Comment on the morphology of the erythrocytes.
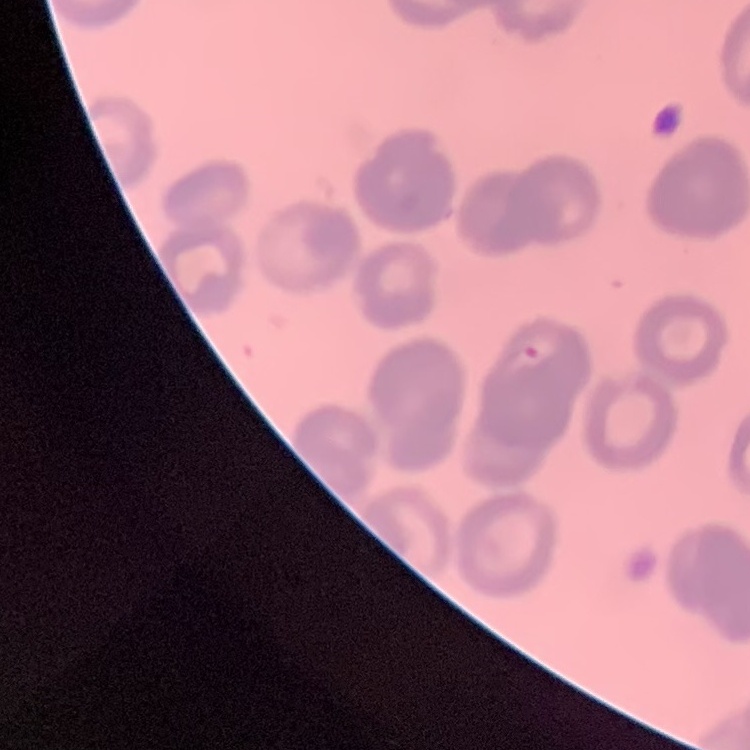

Rouleaux formation.

{
  "preparation": "thin blood smear",
  "stain": "Field's or Giemsa",
  "image_type": "one tile cut from a larger photomicrograph"
}